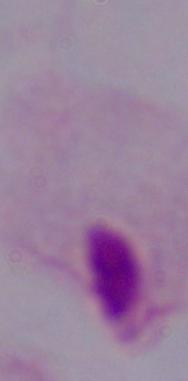 Captured at 1000x magnification. Micrograph. A trichomonad is shown.